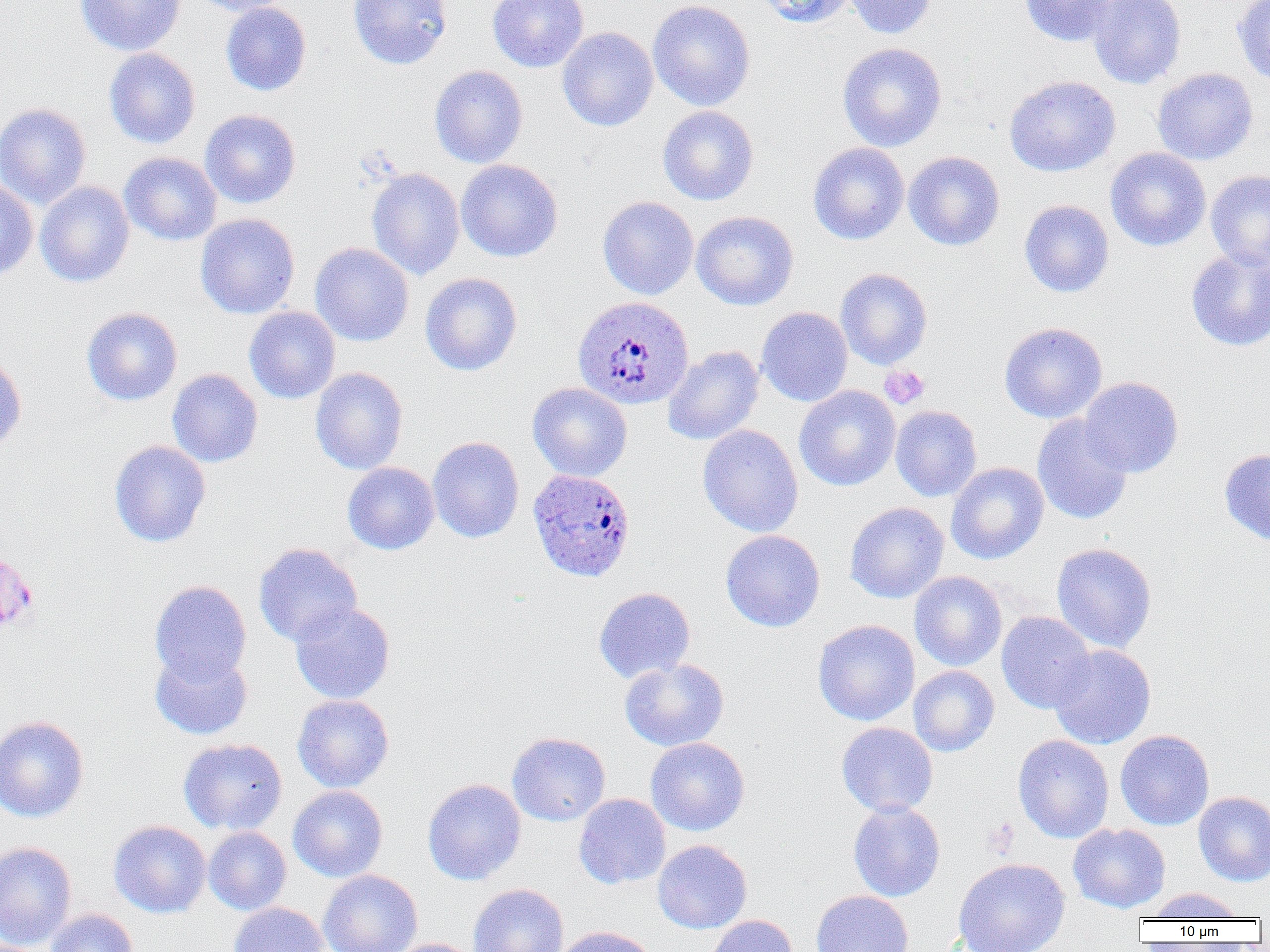
slide-level diagnosis = Plasmodium ovale
image size = 1270×952 pixels
modality = optical microscopy
preparation = thin blood smear
Plasmodium ovale-infected red blood cell locations = approximate bounding boxes as (x1,y1)-(x2,y2) corner pairs in pixels: (572,295)-(694,410), (527,469)-(636,583)
uninfected red blood cell locations = approximate bounding boxes as (x1,y1)-(x2,y2) corner pairs in pixels: (75,0)-(187,56), (192,0)-(294,16), (348,0)-(452,69), (488,0)-(588,72), (646,0)-(756,111), (758,0)-(857,28), (843,0)-(936,39), (1019,0)-(1122,47), (1088,0)-(1186,90), (1232,0)-(1270,88), (220,2)-(311,96), (557,27)-(658,132), (836,42)-(947,152), (103,47)-(201,149), (429,65)-(528,168), (1152,68)-(1258,165), (1004,75)-(1120,176), (0,102)-(91,209), (657,105)-(759,205), (200,109)-(301,209), (807,142)-(910,245), (1105,147)-(1211,251), (903,151)-(1005,251), (119,152)-(222,245), (455,159)-(563,262), (366,167)-(465,280), (1205,169)-(1270,269), (0,180)-(38,281), (35,181)-(134,288), (597,196)-(698,299), (1019,200)-(1114,297), (691,210)-(799,310), (195,213)-(300,319), (310,242)-(414,346), (1186,247)-(1270,351), (835,268)-(933,370), (420,272)-(522,376), (81,306)-(183,406), (756,306)-(853,407), (244,307)-(341,403), (998,321)-(1107,424), (662,345)-(764,445), (0,352)-(27,452), (310,367)-(408,474), (167,369)-(263,467), (1078,377)-(1184,478), (527,382)-(632,481), (794,385)-(901,491), (890,405)-(982,501), (1031,414)-(1133,525), (697,424)-(803,537), (427,436)-(525,543), (109,440)-(211,548), (1219,448)-(1270,545), (342,462)-(439,555), (946,462)-(1049,564), (845,502)-(949,603), (720,530)-(825,632), (1051,542)-(1157,653), (253,543)-(362,646), (909,571)-(1007,671), (149,580)-(252,684), (594,587)-(695,683), (290,603)-(395,704), (996,611)-(1096,714), (813,619)-(919,726), (1049,644)-(1156,749), (150,650)-(253,740), (619,657)-(729,752), (908,665)-(999,757), (292,694)-(394,792), (0,716)-(89,823), (836,722)-(938,817), (1115,730)-(1214,830), (507,732)-(611,826), (1012,734)-(1114,843), (645,737)-(750,835), (178,738)-(288,835), (423,778)-(526,885), (288,785)-(388,881), (1193,791)-(1270,886), (573,793)-(671,889), (848,801)-(946,901), (108,820)-(211,917), (1068,823)-(1171,913), (203,826)-(291,915), (652,840)-(752,934), (0,841)-(77,950), (953,858)-(1070,952), (318,869)-(422,952), (468,884)-(568,952), (1147,887)-(1245,922), (811,890)-(913,952), (228,902)-(329,952), (45,909)-(139,952), (706,915)-(798,952), (551,926)-(657,952), (387,938)-(481,952)
platelet locations = approximate bounding boxes as (x1,y1)-(x2,y2) corner pairs in pixels: (880,366)-(929,409), (983,818)-(1019,858)
magnification = 1000x
field of view = one of a larger specimen